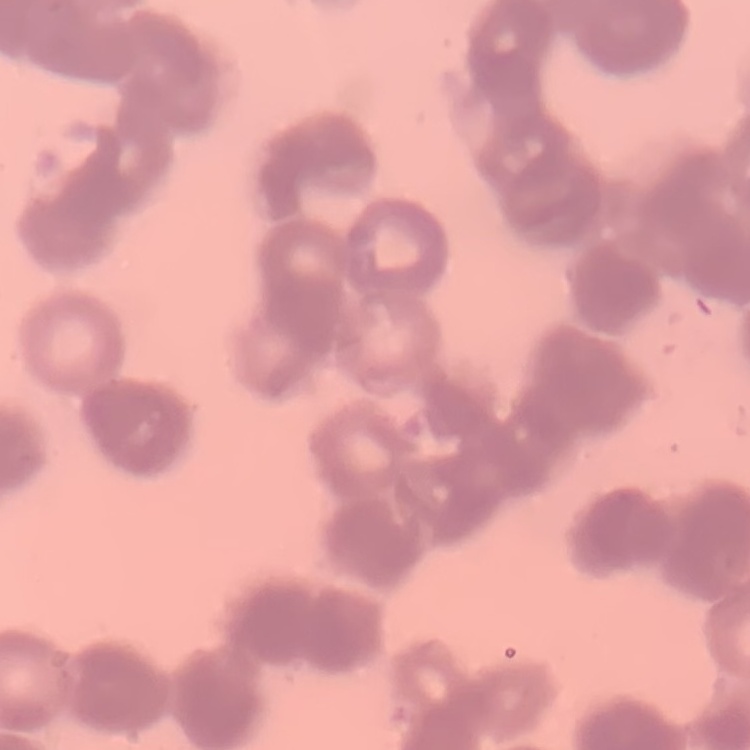
Summary:
  - Red blood cell morphology: rouleaux formation
  - Preparation: thin blood film
  - Stain: Field's or Giemsa
  - Image type: square crop of a larger photomicrograph